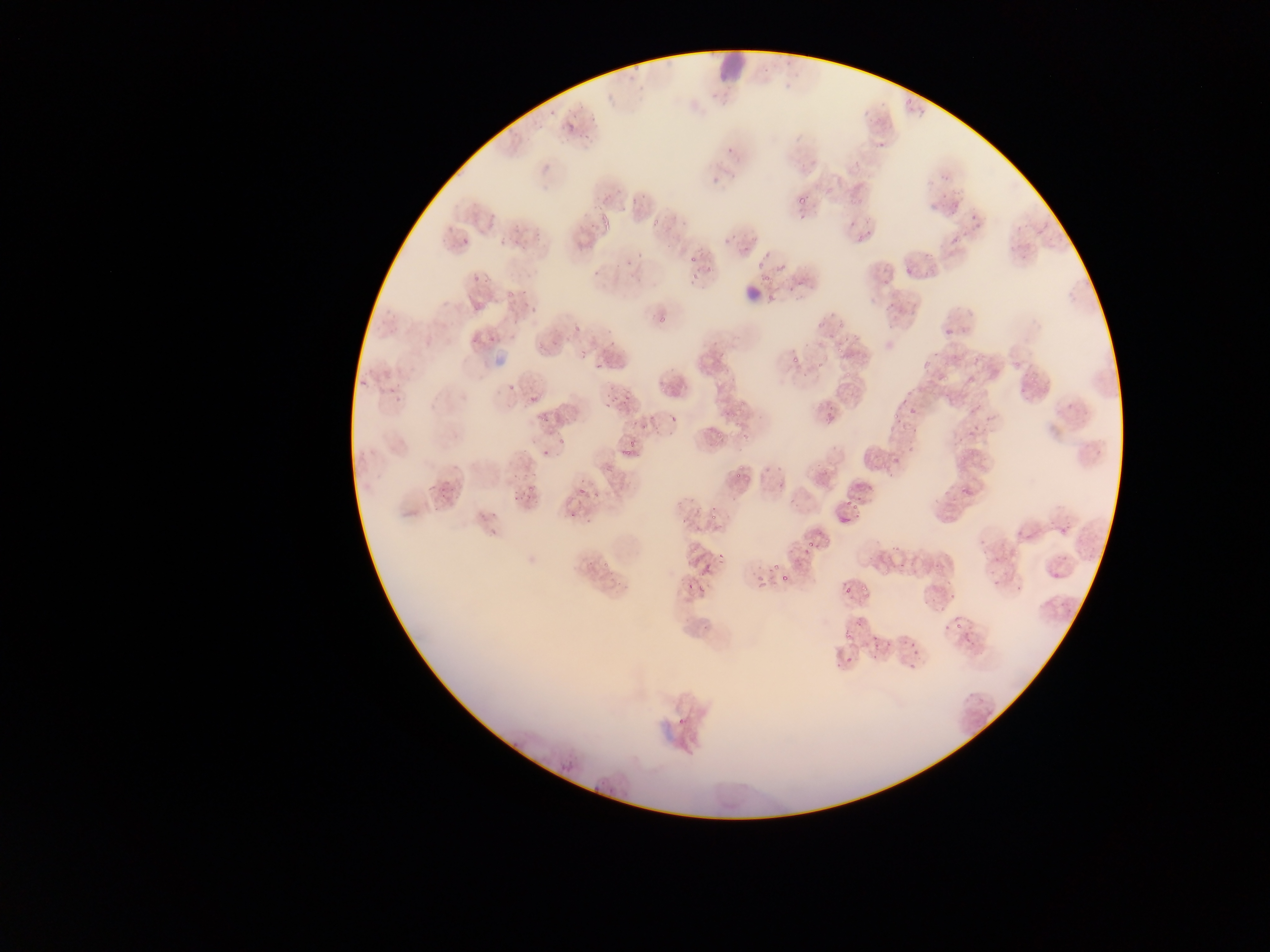

Approximate bounding boxes as {left, top, right, bottom} in pixels.
Summary:
  - Malaria parasite locations: {573, 95, 585, 110}, {901, 96, 915, 108}, {543, 99, 557, 117}, {914, 102, 928, 116}, {529, 119, 537, 130}, {565, 122, 575, 132}, {578, 125, 595, 140}, {509, 126, 519, 145}, {724, 141, 740, 154}, {855, 152, 869, 164}, {711, 169, 725, 180}, {796, 191, 808, 204}, {599, 192, 612, 207}, {628, 192, 645, 211}, {944, 198, 958, 213}, {795, 210, 804, 219}, {646, 212, 666, 226}, {967, 212, 980, 231}, {854, 222, 874, 242}, {948, 233, 960, 246}, {460, 235, 470, 252}, {740, 235, 751, 250}, {579, 240, 589, 250}, {754, 248, 771, 267}, {688, 249, 699, 264}, {624, 254, 641, 270}, {777, 256, 792, 275}, {706, 259, 720, 273}, {904, 264, 917, 278}, {881, 266, 893, 286}, {688, 270, 704, 282}, {784, 280, 796, 297}, {517, 288, 525, 301}, {469, 300, 481, 311}, {881, 302, 893, 315}, {653, 308, 671, 329}, {826, 320, 838, 336}, {570, 324, 578, 335}, {942, 330, 951, 342}, {489, 334, 498, 342}, {537, 336, 550, 349}, {469, 338, 478, 345}, {575, 344, 587, 358}, {834, 348, 841, 358}, {788, 355, 797, 364}, {815, 355, 825, 373}, {593, 358, 603, 370}, {373, 362, 401, 405}, {844, 370, 853, 378}, {508, 384, 517, 393}, {526, 390, 539, 403}, {622, 390, 635, 404}, {604, 391, 623, 406}, {911, 405, 918, 415}, {827, 408, 832, 418}, {538, 411, 550, 423}, {889, 413, 901, 421}, {665, 417, 677, 427}, {625, 421, 648, 429}, {740, 428, 749, 438}, {556, 434, 566, 448}, {620, 442, 633, 456}, {890, 452, 898, 466}, {516, 458, 535, 480}, {777, 461, 788, 479}, {732, 467, 743, 478}, {955, 479, 976, 500}, {525, 485, 535, 499}, {578, 486, 586, 495}, {594, 487, 600, 499}, {788, 489, 799, 503}, {682, 498, 696, 526}, {844, 498, 857, 514}, {710, 509, 719, 523}, {569, 510, 577, 522}, {802, 536, 818, 554}, {891, 543, 901, 552}, {793, 551, 803, 564}, {716, 552, 727, 565}, {602, 559, 609, 568}, {768, 563, 777, 574}, {698, 565, 709, 575}, {883, 568, 887, 577}, {782, 571, 789, 580}, {753, 573, 771, 592}, {687, 581, 697, 594}, {949, 582, 964, 601}, {844, 585, 851, 596}, {924, 585, 942, 605}, {860, 586, 869, 604}, {855, 618, 865, 629}, {955, 619, 963, 631}, {903, 632, 920, 650}, {875, 636, 885, 658}, {844, 657, 854, 663}, {901, 660, 915, 675} | approximate {x, y} pixel centers of objects too small to bound: {503, 241}, {474, 279}
  - Leukocyte locations: {719, 49, 750, 83}, {735, 281, 763, 307}
  - Image size: 1270×952 pixels
  - Field of view: single
  - Capture: mobile-phone photograph through a microscope
  - Preparation: thin blood film
  - Country: Ghana